Name the blood parasite species.
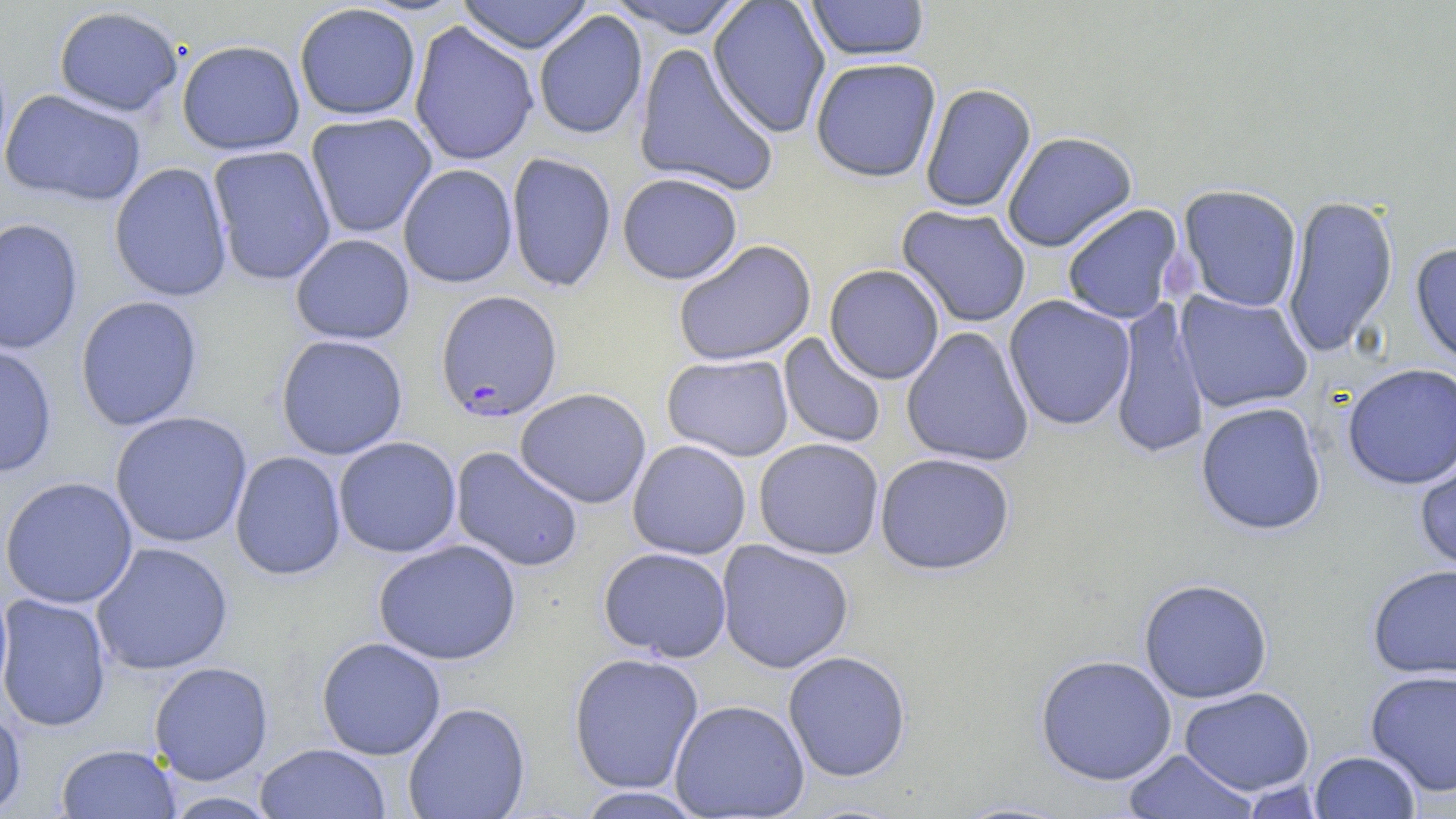
Plasmodium falciparum.

field of view = single
Plasmodium falciparum-infected red blood cell locations = approximate bounding boxes as (x1, y1, x2, y2) in pixels: (435, 289, 563, 422)
modality = optical microscopy
stain = May-Grünwald-Giemsa
preparation = thin blood film
uninfected red blood cell locations = approximate bounding boxes as (x1, y1, x2, y2) in pixels: (457, 0, 594, 54), (605, 0, 751, 38), (707, 0, 831, 139), (805, 0, 930, 61), (294, 3, 421, 121), (53, 5, 184, 117), (533, 10, 648, 140), (408, 20, 539, 167), (176, 39, 305, 156), (633, 43, 779, 197), (810, 57, 941, 182), (919, 83, 1036, 214), (1, 89, 146, 206), (305, 112, 437, 239), (1001, 131, 1138, 252), (207, 145, 336, 286), (505, 152, 617, 293), (109, 161, 233, 302), (397, 163, 518, 288), (617, 172, 743, 284), (1177, 184, 1303, 313), (1281, 193, 1399, 358), (896, 204, 1031, 328), (1061, 204, 1185, 324), (0, 217, 84, 355), (290, 233, 415, 345), (672, 239, 816, 367), (1410, 241, 1456, 368), (824, 264, 945, 385), (1174, 290, 1313, 414), (75, 295, 203, 431), (1003, 295, 1136, 431), (1109, 298, 1210, 461), (901, 326, 1035, 468), (778, 332, 887, 449), (275, 334, 409, 460), (0, 343, 57, 478), (662, 353, 794, 462), (1341, 362, 1456, 490), (514, 387, 652, 508), (1195, 401, 1327, 535), (109, 411, 253, 548), (333, 436, 461, 558), (753, 438, 884, 560), (627, 439, 751, 560), (450, 446, 585, 573), (1414, 446, 1456, 579), (229, 450, 346, 580), (874, 452, 1015, 575), (0, 476, 139, 609), (373, 539, 521, 666), (716, 539, 855, 674), (91, 541, 233, 675), (598, 547, 732, 662), (1367, 563, 1456, 679), (1138, 578, 1273, 703), (0, 593, 112, 732), (316, 637, 446, 759), (782, 650, 911, 782), (568, 651, 704, 795), (1034, 654, 1177, 786), (149, 661, 273, 785), (1364, 668, 1456, 797), (1179, 687, 1315, 795), (669, 699, 810, 818), (403, 702, 530, 819), (0, 705, 27, 816), (254, 743, 390, 819), (55, 744, 181, 818), (1122, 748, 1260, 818), (1308, 750, 1422, 818), (574, 786, 707, 818)
image size = 1456×819 pixels
magnification = 1000x